Assess this cell for malaria.
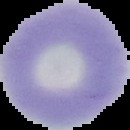
It is uninfected.

preparation = thin blood smear
image type = segmented cell region with the area outside set to black
image size = 130×130 pixels